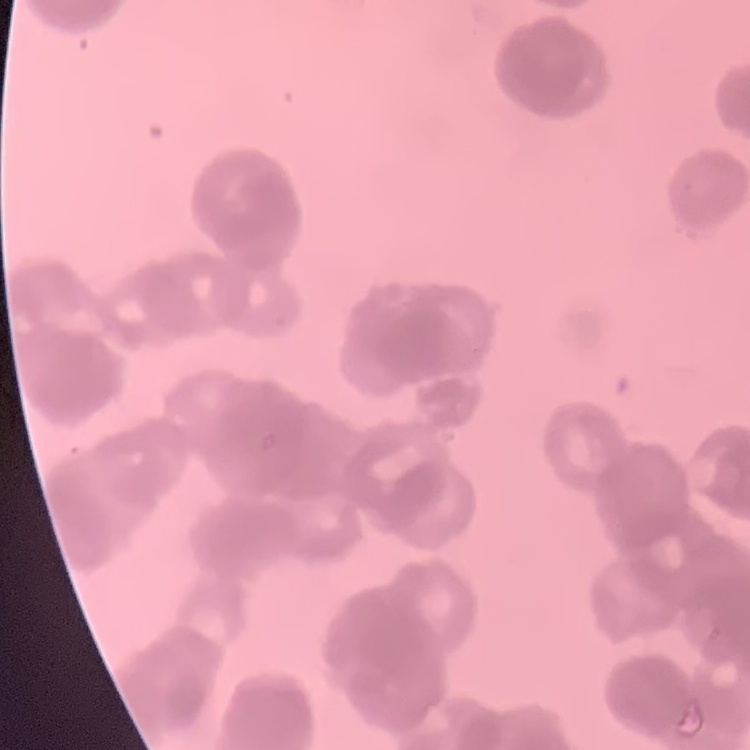
erythrocyte_morphology: rouleaux formation
image_type: one tile cut from a larger photomicrograph
stain: Field's or Giemsa
preparation: thin blood film